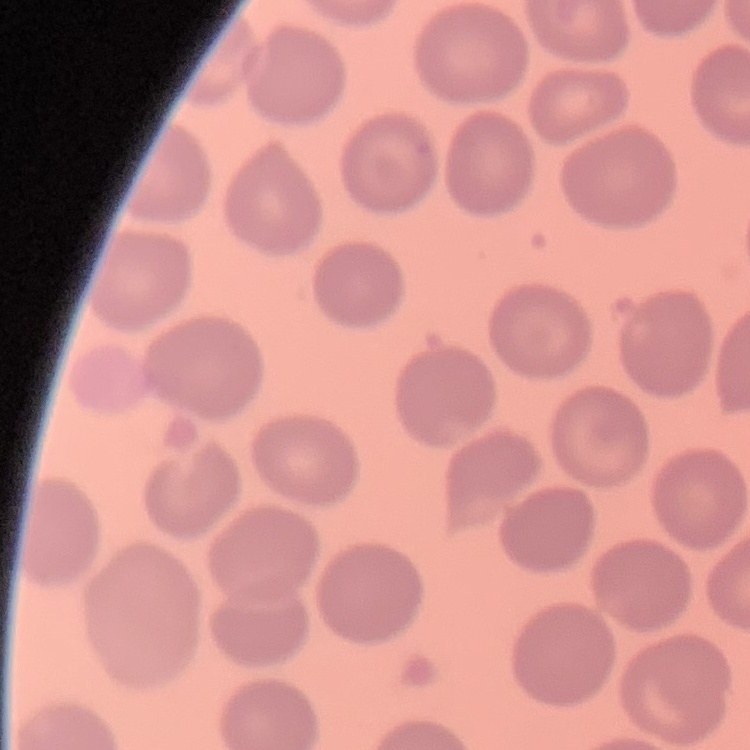
Summary:
  - Red blood cell morphology: no rouleaux formation
  - Preparation: thin peripheral smear
  - Image type: one tile cut from a larger photomicrograph
  - Stain: Field's or Giemsa